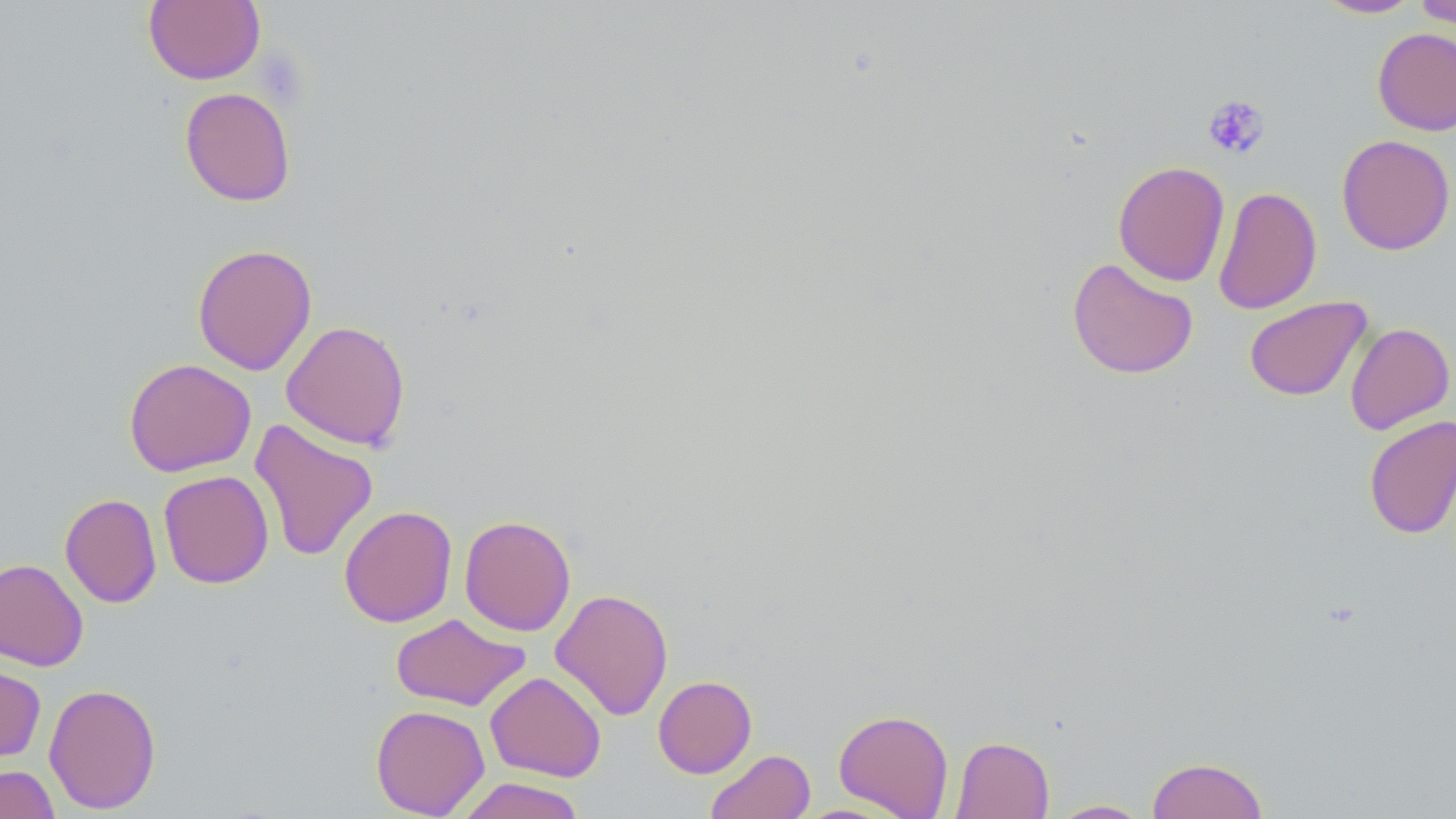

Approximate bounding boxes as (x1,y1)-(x2,y2) corner pairs in pixels. Uninfected red blood cell locations: (143,0)-(265,85), (1315,0)-(1423,18), (1414,0)-(1456,31), (1372,27)-(1456,136), (179,86)-(296,207), (1337,134)-(1455,255), (1113,160)-(1230,287), (1213,186)-(1322,315), (192,243)-(318,375), (1067,257)-(1199,380), (1243,296)-(1372,401), (281,320)-(411,451), (1344,322)-(1455,435), (123,358)-(256,477), (1363,414)-(1456,540), (249,418)-(379,561), (159,470)-(274,588), (60,493)-(161,608), (339,505)-(457,627), (459,515)-(576,636), (0,558)-(89,671), (550,588)-(674,721), (390,613)-(530,711), (0,660)-(46,765), (485,671)-(606,782), (653,675)-(757,778), (43,682)-(162,815), (370,705)-(490,818), (833,709)-(954,818), (950,736)-(1055,819), (706,749)-(815,819), (1147,756)-(1268,819), (0,764)-(61,819), (456,776)-(586,819), (1048,799)-(1153,818). Platelet locations: (1203,94)-(1270,160). Slide-level diagnosis: negative for blood parasites. Image is 1456×819 pixels. Thin blood film. Single field of view. Captured at 1000x magnification. May-Grünwald-Giemsa stain. Light microscopy.